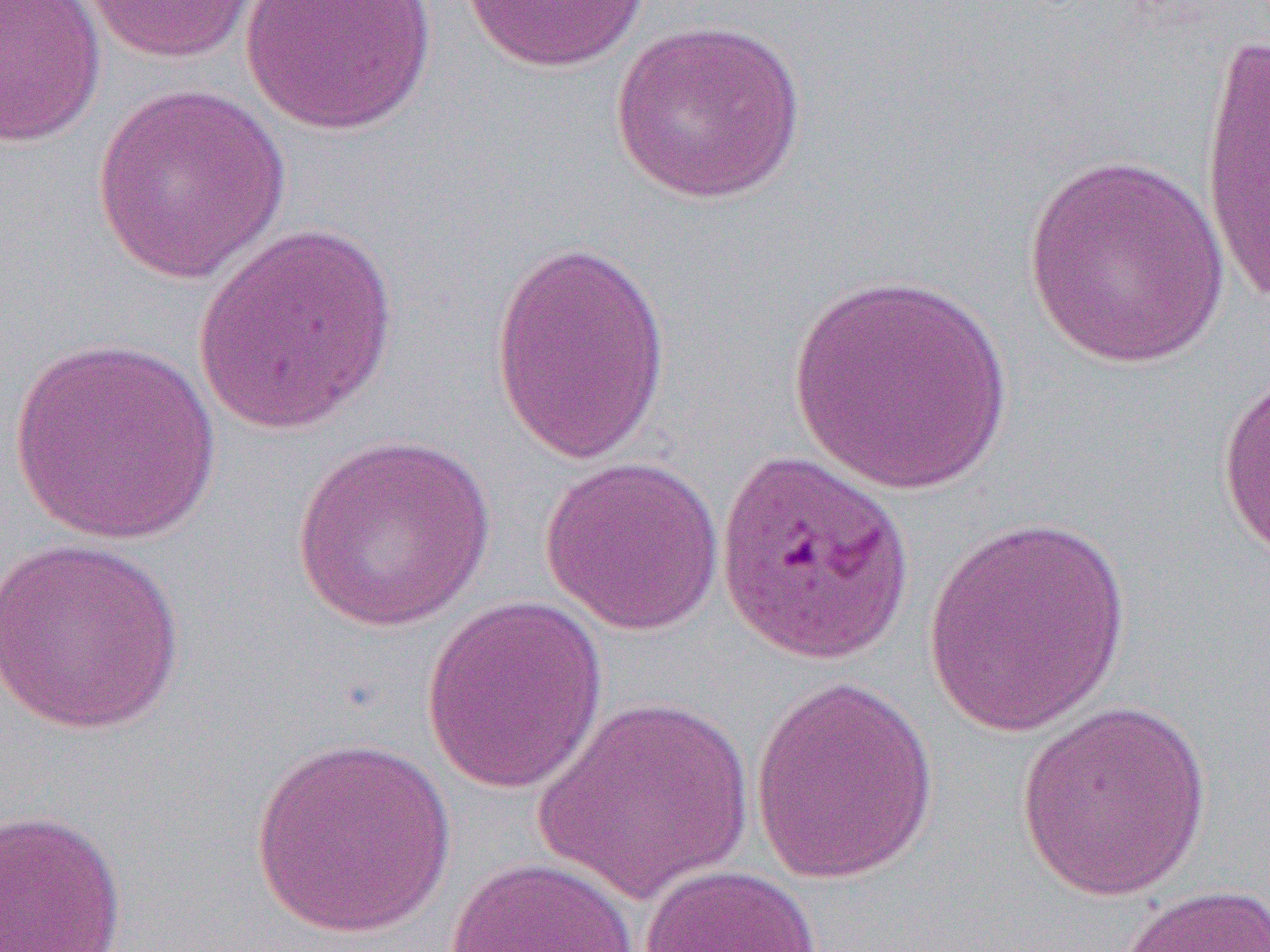
slide-level diagnosis = Plasmodium falciparum
magnification = 1000x
preparation = thin blood smear
uninfected red blood cell locations = approximate bounding boxes as (x1, y1, x2, y2) in pixels: (0, 0, 105, 147), (80, 0, 263, 64), (240, 0, 438, 136), (460, 0, 651, 73), (610, 19, 807, 206), (1197, 26, 1270, 310), (91, 84, 292, 285), (1020, 153, 1232, 371), (191, 224, 400, 437), (489, 240, 671, 464), (786, 271, 1016, 496), (7, 337, 223, 545), (1217, 367, 1270, 570), (291, 434, 496, 634), (538, 456, 726, 636), (921, 513, 1135, 737), (0, 535, 187, 737), (421, 596, 609, 794), (748, 676, 939, 884), (532, 695, 757, 905), (1015, 701, 1215, 901), (248, 736, 457, 937), (0, 808, 128, 951), (443, 856, 641, 952), (637, 863, 821, 952), (1112, 884, 1270, 952)
image size = 1270×952 pixels
field of view = one of a larger specimen
modality = optical microscopy